Give the position of every Plasmodium parasite, noting whether each is a trophozoite, schizont, or gametocyte.
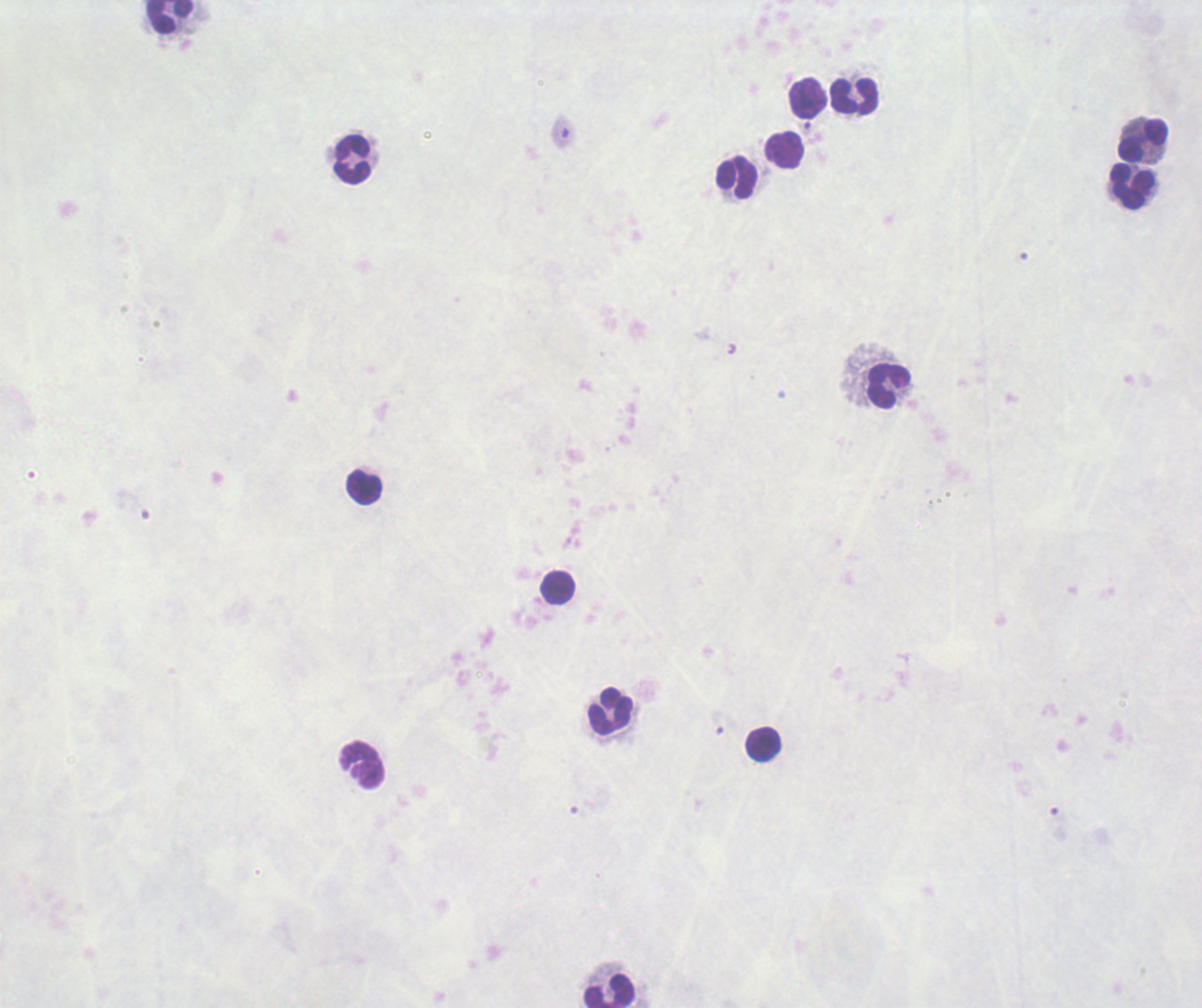

No Plasmodium parasites detected.

Approximate object centers, in pixels from the top-left corner. Leukocyte locations: (x=169, y=17), (x=854, y=97), (x=808, y=98), (x=1143, y=141), (x=786, y=149), (x=353, y=159), (x=737, y=177), (x=1133, y=186), (x=889, y=386), (x=365, y=488), (x=558, y=589), (x=611, y=712), (x=763, y=745), (x=362, y=765), (x=610, y=992). Captured at 100x magnification. Background quality: unsatisfactory. Previously used in a real diagnosis. Thick blood smear. Romanowsky stain. Image is 1202×1008 pixels. One field from this slide.